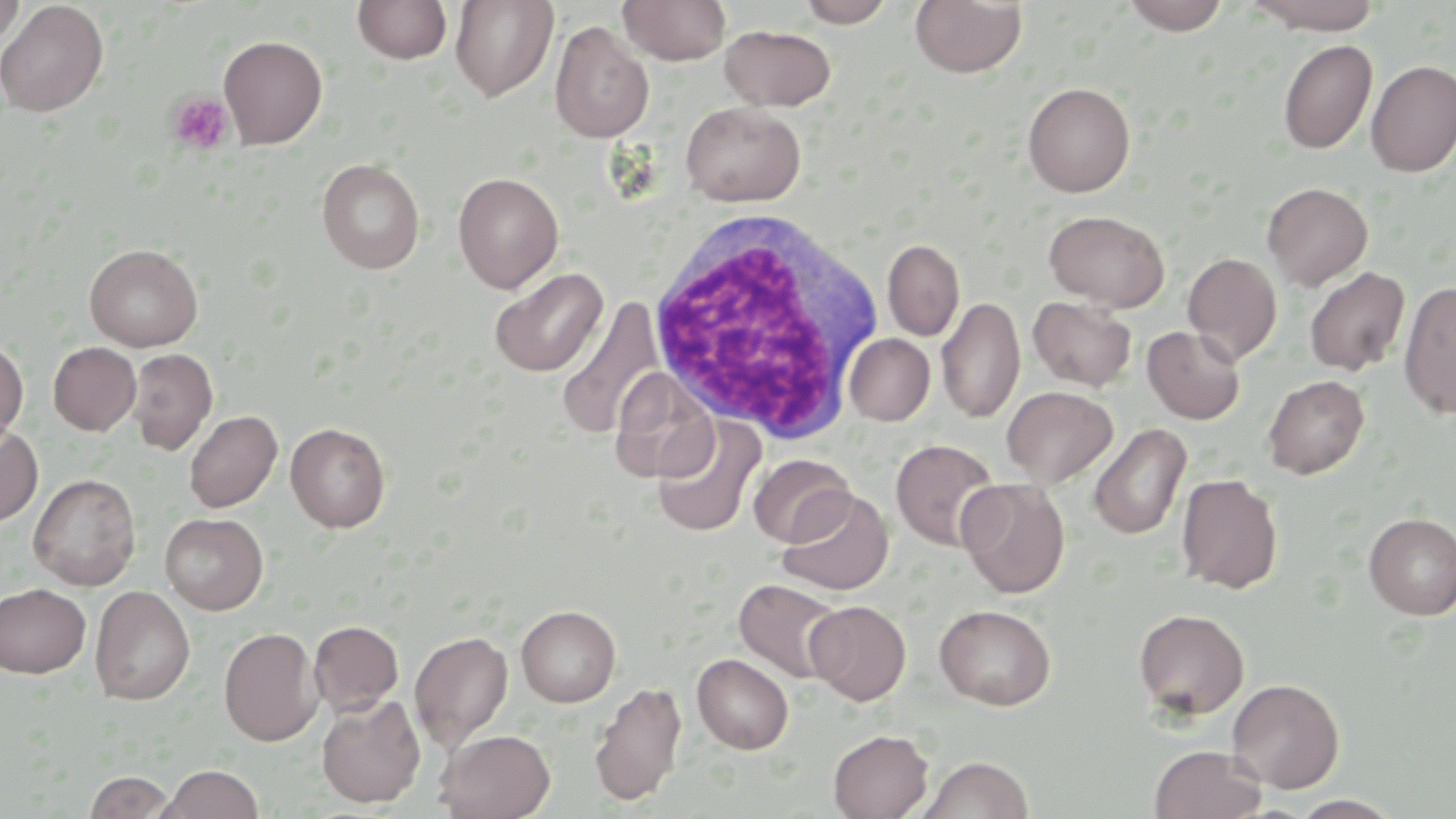
slide-level diagnosis = no evidence of blood parasites
white blood cell locations = approximate bounding boxes as named x1/y1/x2/y2 corners in pixels: (x1=645, y1=209, x2=888, y2=444)
field of view = single
stain = May-Grünwald-Giemsa
uninfected red blood cell locations = approximate bounding boxes as named x1/y1/x2/y2 corners in pixels: (x1=0, y1=0, x2=26, y2=48), (x1=449, y1=0, x2=559, y2=102), (x1=618, y1=0, x2=731, y2=65), (x1=1121, y1=0, x2=1230, y2=35), (x1=1246, y1=0, x2=1384, y2=34), (x1=0, y1=1, x2=108, y2=117), (x1=352, y1=1, x2=453, y2=66), (x1=795, y1=1, x2=897, y2=27), (x1=910, y1=1, x2=1027, y2=78), (x1=550, y1=21, x2=654, y2=143), (x1=720, y1=25, x2=836, y2=111), (x1=219, y1=35, x2=327, y2=149), (x1=1278, y1=39, x2=1378, y2=154), (x1=1365, y1=60, x2=1456, y2=176), (x1=1022, y1=81, x2=1136, y2=197), (x1=681, y1=101, x2=805, y2=206), (x1=316, y1=158, x2=425, y2=273), (x1=452, y1=172, x2=563, y2=293), (x1=1262, y1=182, x2=1373, y2=290), (x1=1044, y1=209, x2=1169, y2=311), (x1=883, y1=239, x2=964, y2=341), (x1=84, y1=243, x2=203, y2=351), (x1=1183, y1=252, x2=1282, y2=365), (x1=489, y1=267, x2=608, y2=377), (x1=1304, y1=267, x2=1410, y2=376), (x1=1398, y1=281, x2=1456, y2=418), (x1=937, y1=295, x2=1025, y2=424), (x1=1027, y1=296, x2=1138, y2=392), (x1=557, y1=298, x2=665, y2=440), (x1=1142, y1=325, x2=1246, y2=424), (x1=844, y1=333, x2=935, y2=426), (x1=0, y1=338, x2=28, y2=446), (x1=48, y1=342, x2=141, y2=435), (x1=127, y1=348, x2=218, y2=455), (x1=609, y1=368, x2=718, y2=483), (x1=1262, y1=374, x2=1369, y2=478), (x1=1002, y1=386, x2=1118, y2=487), (x1=184, y1=410, x2=282, y2=513), (x1=652, y1=416, x2=765, y2=537), (x1=0, y1=422, x2=43, y2=527), (x1=285, y1=422, x2=390, y2=532), (x1=1088, y1=423, x2=1191, y2=540), (x1=890, y1=438, x2=1001, y2=551), (x1=748, y1=453, x2=855, y2=548), (x1=28, y1=473, x2=141, y2=590), (x1=1177, y1=473, x2=1283, y2=594), (x1=957, y1=479, x2=1070, y2=598), (x1=778, y1=487, x2=893, y2=595), (x1=161, y1=513, x2=268, y2=614), (x1=1363, y1=513, x2=1456, y2=619), (x1=734, y1=578, x2=846, y2=683), (x1=0, y1=583, x2=90, y2=677), (x1=90, y1=585, x2=195, y2=705), (x1=806, y1=600, x2=911, y2=704), (x1=516, y1=605, x2=621, y2=707), (x1=934, y1=605, x2=1056, y2=710), (x1=1134, y1=608, x2=1249, y2=720), (x1=309, y1=621, x2=403, y2=716), (x1=307, y1=624, x2=501, y2=728), (x1=219, y1=626, x2=322, y2=746), (x1=410, y1=630, x2=513, y2=751), (x1=692, y1=654, x2=794, y2=754), (x1=1227, y1=678, x2=1344, y2=793), (x1=589, y1=681, x2=687, y2=806), (x1=316, y1=694, x2=425, y2=808), (x1=435, y1=729, x2=555, y2=819), (x1=828, y1=729, x2=933, y2=819), (x1=1149, y1=745, x2=1267, y2=819), (x1=918, y1=756, x2=1034, y2=819), (x1=156, y1=764, x2=263, y2=819), (x1=84, y1=771, x2=176, y2=818), (x1=1289, y1=794, x2=1403, y2=818)
platelet locations = approximate bounding boxes as named x1/y1/x2/y2 corners in pixels: (x1=166, y1=91, x2=235, y2=155)
magnification = 1000x
modality = optical microscopy
preparation = thin blood smear
image size = 1456×819 pixels